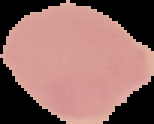
{
  "preparation": "thin blood smear",
  "image_size": "154×124 pixels",
  "malaria_status": "uninfected",
  "image_type": "segmented cell region with the area outside set to black"
}